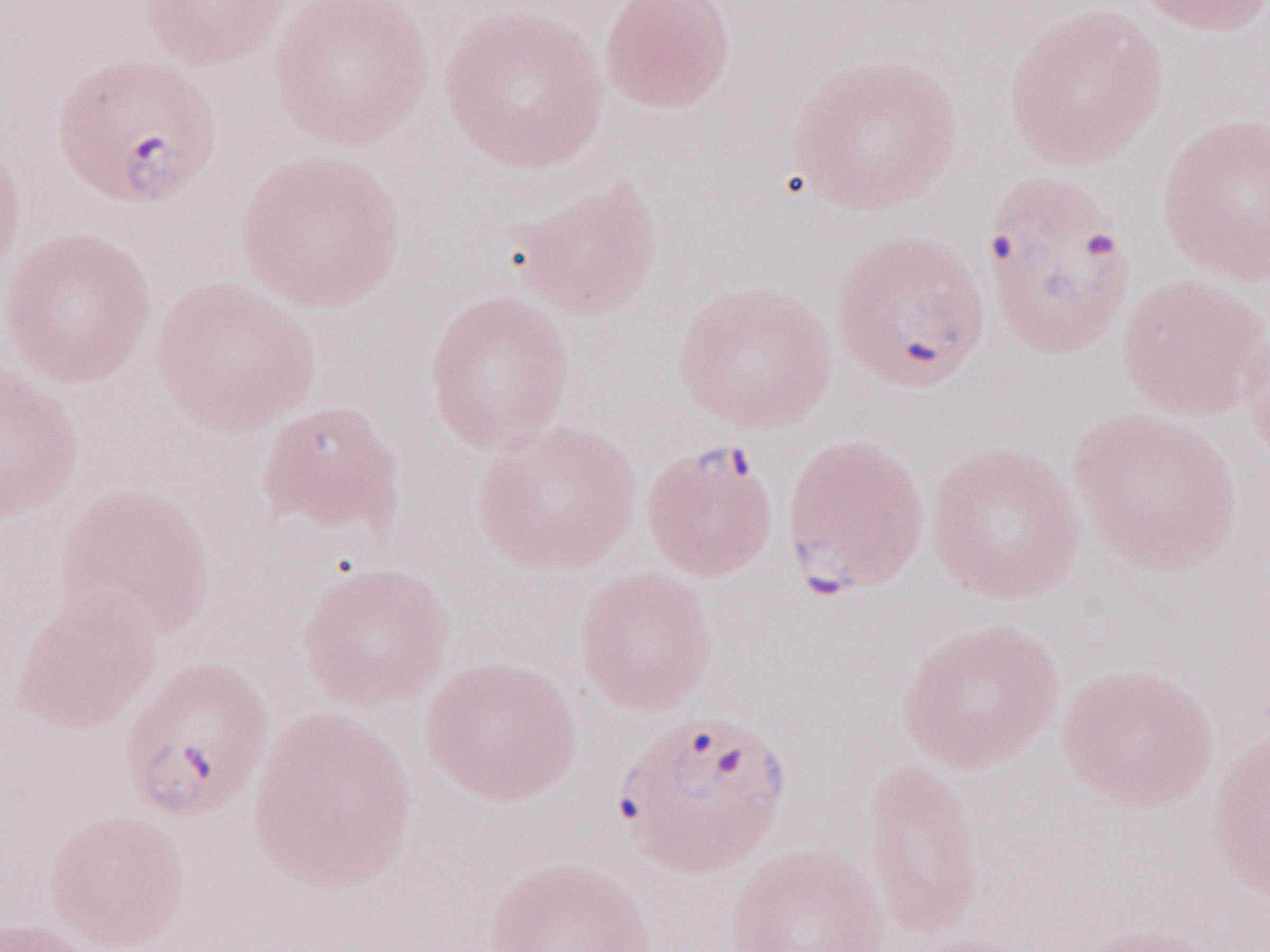 Magnification: 1,000x. Single field of view. Olympus BX43 microscope, Olympus DP73 camera. May-Grünwald-Giemsa-stained preparation. Thin peripheral-blood smear. Patient-level malaria diagnosis: positive. Image is 1270×952 pixels.